Classify this cell by malaria status.
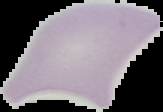
Uninfected.

Summary:
  - Image size: 163×112 pixels
  - Preparation: thin blood smear
  - Image type: segmented cell region with the area outside set to black